State which parasite is depicted.
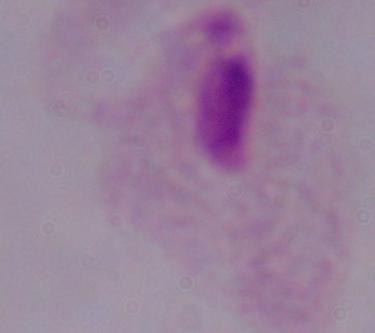
A trichomonad.

modality = photomicrograph
magnification = 1000x